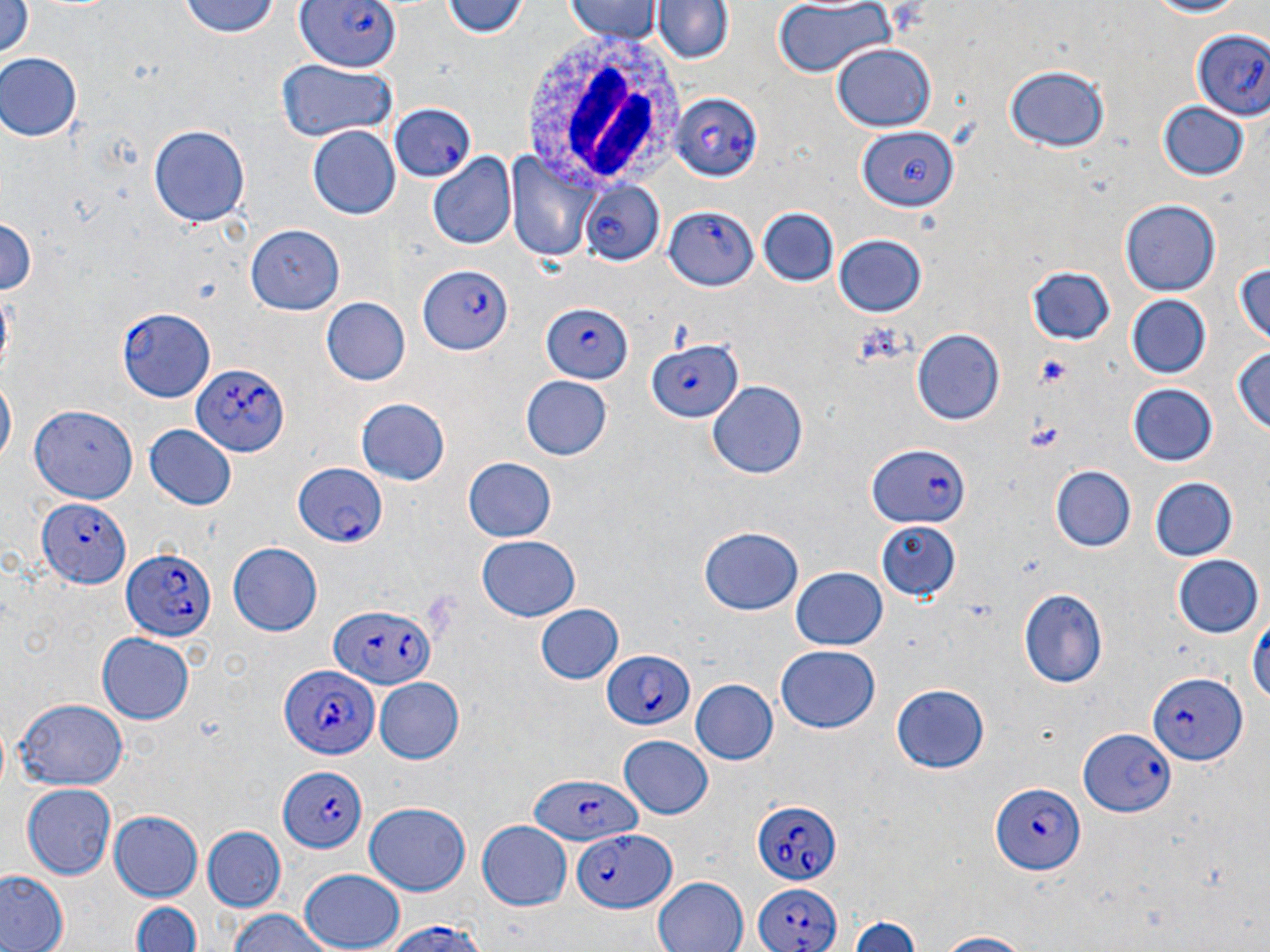
slide-level diagnosis = Plasmodium falciparum
preparation = thin blood film
uninfected red blood cell locations = approximate bounding boxes as (x1,y1)-(x2,y2) corner pairs in pixels: (179,0)-(282,40), (445,0)-(528,40), (1138,0)-(1250,18), (566,1)-(662,43), (649,1)-(733,68), (772,1)-(894,81), (1,2)-(32,65), (828,43)-(936,133), (1,52)-(83,142), (276,58)-(398,142), (1006,65)-(1109,152), (1157,101)-(1248,182), (149,122)-(248,225), (307,125)-(399,218), (858,130)-(959,214), (507,147)-(598,265), (426,154)-(516,252), (1119,199)-(1221,297), (758,206)-(837,286), (0,215)-(38,300), (247,222)-(341,314), (832,234)-(928,318), (1233,260)-(1270,352), (1026,265)-(1115,345), (1123,292)-(1214,380), (323,296)-(410,386), (912,327)-(1005,425), (1231,343)-(1269,441), (1,375)-(15,471), (521,377)-(612,461), (708,379)-(807,476), (1127,383)-(1218,467), (356,398)-(451,485), (30,406)-(140,500), (144,423)-(237,509), (462,455)-(557,541), (1051,465)-(1135,552), (1151,477)-(1237,562), (880,518)-(961,601), (699,526)-(804,615), (478,538)-(580,621), (228,541)-(323,636), (1172,554)-(1265,640), (791,565)-(889,651), (1015,589)-(1109,688), (534,604)-(624,685), (1248,607)-(1268,719), (97,635)-(193,722), (774,646)-(881,733), (373,677)-(464,764), (690,679)-(779,766), (891,683)-(991,772), (12,699)-(128,790), (618,735)-(715,818), (23,784)-(118,878), (362,802)-(471,896), (107,809)-(205,902), (478,819)-(573,910), (201,826)-(287,913), (0,869)-(68,952), (297,869)-(405,951), (650,875)-(748,952), (130,899)-(202,951), (220,909)-(336,952), (852,916)-(921,952), (929,931)-(1046,951)
image size = 1270×952 pixels
platelet locations = approximate bounding boxes as (x1,y1)-(x2,y2) corner pairs in pixels: (852,324)-(908,368), (1035,354)-(1074,389), (1023,421)-(1065,454)
magnification = 1000x
field of view = one of a larger specimen
Plasmodium falciparum-infected red blood cell locations = approximate bounding boxes as (x1,y1)-(x2,y2) corner pairs in pixels: (292,0)-(407,72), (1194,30)-(1270,117), (671,91)-(765,183), (389,100)-(475,182), (579,177)-(661,263), (664,205)-(757,292), (419,265)-(513,357), (542,302)-(634,381), (117,307)-(216,402), (644,339)-(741,424), (190,365)-(291,456), (866,446)-(971,528), (291,463)-(386,549), (39,496)-(129,587), (122,547)-(214,643), (331,604)-(432,690), (600,648)-(698,731), (277,665)-(377,761), (1149,673)-(1246,765), (1076,727)-(1176,818), (277,766)-(371,853), (521,777)-(640,844), (993,780)-(1085,875), (753,798)-(841,886), (575,829)-(675,912), (751,877)-(842,952), (375,921)-(493,952)
white blood cell locations = approximate bounding boxes as (x1,y1)-(x2,y2) corner pairs in pixels: (518,31)-(687,195)
stain = May-Grünwald-Giemsa
modality = light microscopy